State the preparation type.
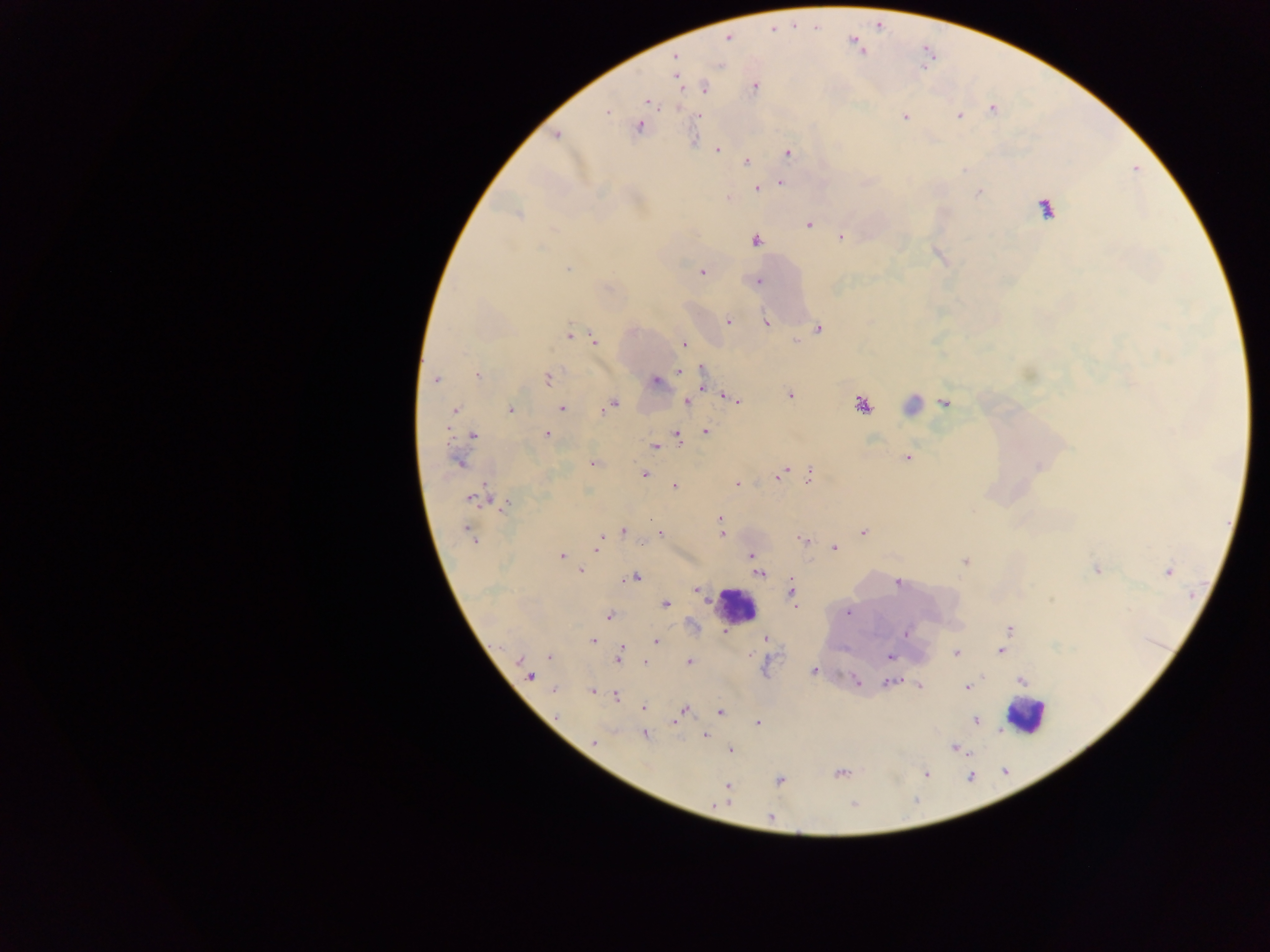

Thick blood film.

image_size: 1270×952 pixels
country: Ghana
field_of_view: single
leukocyte_locations: 'approximate centers as (x, y) in pixels: (735, 606), (1025, 714)'
malaria_parasite_locations: 'approximate centers as (x, y) in pixels: (727, 38), (675, 57), (755, 86), (704, 88), (648, 101), (993, 110), (606, 111), (958, 115), (700, 116), (905, 117), (639, 127), (556, 135), (717, 150), (789, 152), (746, 161), (781, 183), (757, 188), (979, 192), (728, 198), (1045, 208), (517, 214), (809, 224), (841, 237), (756, 241), (567, 269), (702, 273), (758, 281), (728, 321), (766, 323), (819, 327), (569, 335), (594, 339), (684, 344), (679, 371), (477, 374), (548, 377), (702, 378), (435, 379), (655, 381), (790, 396), (733, 399), (687, 401), (945, 403), (613, 405), (862, 405), (606, 407), (561, 409), (454, 411), (510, 411), (705, 432), (473, 435), (546, 435), (677, 437), (655, 446), (906, 458), (459, 461), (593, 464), (809, 473), (645, 474), (779, 476), (737, 484), (674, 486), (474, 499), (505, 504), (720, 518), (623, 531), (863, 532), (660, 533), (723, 534), (470, 536), (803, 540), (599, 542), (641, 544), (834, 548), (562, 556), (751, 556), (965, 562), (1096, 570), (581, 571), (1168, 571), (759, 574), (636, 577), (898, 583), (696, 590), (792, 591), (666, 604), (848, 613), (608, 616), (1010, 628), (725, 632), (906, 633), (765, 638), (1005, 639), (592, 641), (656, 641), (621, 650), (1001, 652), (956, 653), (549, 657), (890, 657), (518, 658), (618, 658), (689, 662), (645, 663), (813, 670), (529, 676), (856, 681), (1022, 681), (891, 683), (919, 685), (967, 687), (554, 690), (592, 691), (615, 696), (644, 707), (684, 709), (720, 712), (557, 716), (675, 720), (975, 720), (757, 723), (644, 734), (705, 736), (594, 742), (956, 748), (730, 750), (839, 773), (926, 774), (779, 781), (728, 786), (854, 804), (770, 817)'
capture: mobile-phone photograph through a microscope